Assess this cell for malaria.
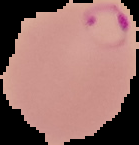

It is parasitized.

Summary:
  - Image size: 139×145 pixels
  - Image type: cell region segmented out of the field of view; surrounding area masked to black
  - Preparation: thin blood smear